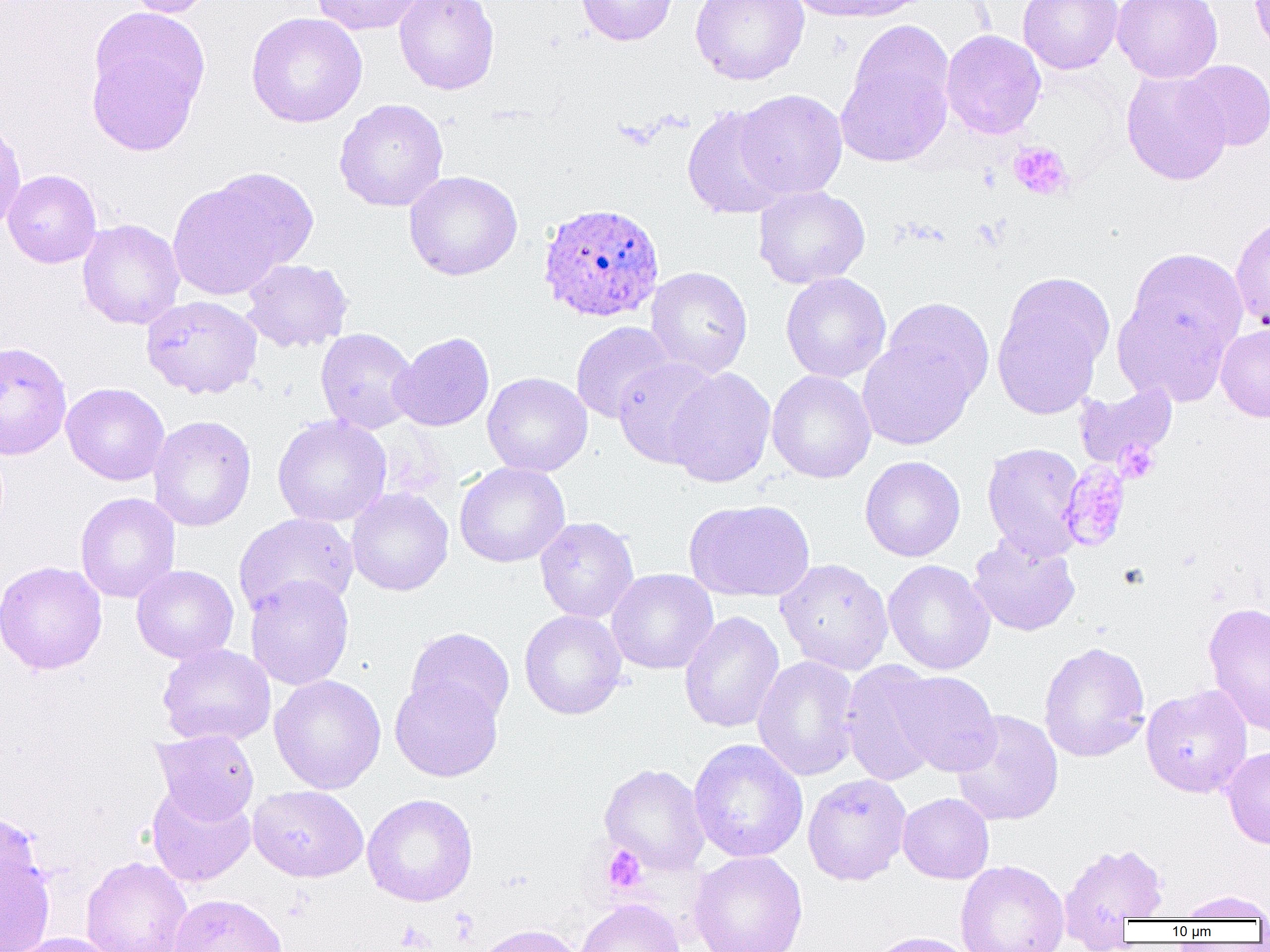

slide_level_diagnosis: Plasmodium ovale
uninfected_red_blood_cell_locations: 'approximate bounding boxes as [x1, y1, x2, y2] in pixels: [120, 0, 218, 17], [311, 0, 425, 36], [394, 0, 499, 95], [575, 0, 680, 46], [690, 0, 809, 85], [784, 0, 924, 23], [1018, 0, 1123, 74], [1112, 0, 1223, 83], [1251, 0, 1270, 58], [85, 8, 210, 155], [246, 12, 367, 128], [940, 29, 1046, 140], [836, 36, 954, 167], [1179, 60, 1270, 151], [1121, 69, 1232, 185], [735, 89, 848, 200], [334, 98, 448, 212], [682, 104, 792, 220], [0, 116, 26, 233], [3, 169, 101, 268], [404, 170, 523, 280], [168, 174, 306, 300], [753, 185, 870, 289], [1230, 214, 1270, 332], [77, 219, 185, 330], [1124, 247, 1249, 371], [242, 259, 353, 353], [646, 266, 753, 377], [780, 272, 892, 383], [991, 275, 1110, 420], [141, 295, 262, 399], [1113, 295, 1235, 405], [881, 297, 995, 409], [571, 321, 676, 424], [1216, 324, 1270, 421], [315, 328, 419, 434], [390, 331, 495, 432], [857, 333, 978, 451], [613, 357, 723, 469], [665, 367, 776, 488], [767, 370, 876, 484], [482, 372, 592, 477], [1073, 382, 1179, 473], [61, 383, 169, 485], [148, 415, 256, 532], [272, 415, 392, 527], [982, 442, 1086, 559], [860, 456, 965, 562], [454, 462, 570, 568], [346, 487, 454, 596], [75, 492, 180, 603], [684, 499, 815, 602], [234, 514, 358, 618], [535, 517, 639, 623], [968, 534, 1080, 636], [775, 558, 894, 675], [883, 559, 995, 675], [0, 560, 107, 675], [131, 564, 239, 664], [607, 569, 718, 675], [245, 575, 354, 691], [1203, 601, 1270, 737], [519, 610, 628, 720], [678, 611, 785, 733], [405, 628, 514, 727], [1038, 641, 1150, 762], [157, 643, 275, 746], [752, 655, 861, 781], [840, 661, 946, 787], [891, 670, 1000, 777], [269, 674, 386, 794], [390, 674, 503, 782], [1140, 684, 1253, 798], [952, 710, 1064, 826], [152, 729, 259, 824], [688, 738, 808, 863], [1220, 746, 1270, 849], [600, 763, 709, 875], [802, 773, 912, 885], [145, 782, 256, 887], [247, 784, 368, 882], [897, 792, 994, 884], [362, 793, 478, 906], [0, 813, 45, 909], [1059, 841, 1169, 933], [0, 842, 55, 952], [688, 851, 808, 952], [81, 856, 192, 952], [955, 860, 1069, 952], [1175, 890, 1270, 921], [168, 893, 289, 952], [574, 898, 686, 952], [470, 923, 584, 952], [866, 931, 978, 952], [9, 933, 118, 952]'
image_size: 1270×952 pixels
field_of_view: one of a larger specimen
plasmodium_ovale_infected_red_blood_cell_locations: 'approximate bounding boxes as [x1, y1, x2, y2] in pixels: [537, 202, 664, 323], [0, 341, 72, 460]'
platelet_locations: 'approximate bounding boxes as [x1, y1, x2, y2] in pixels: [1008, 142, 1073, 201], [1115, 440, 1160, 483], [1058, 462, 1131, 552], [602, 846, 647, 893], [395, 922, 434, 951]'
modality: optical microscopy
preparation: thin blood smear
magnification: 1000x